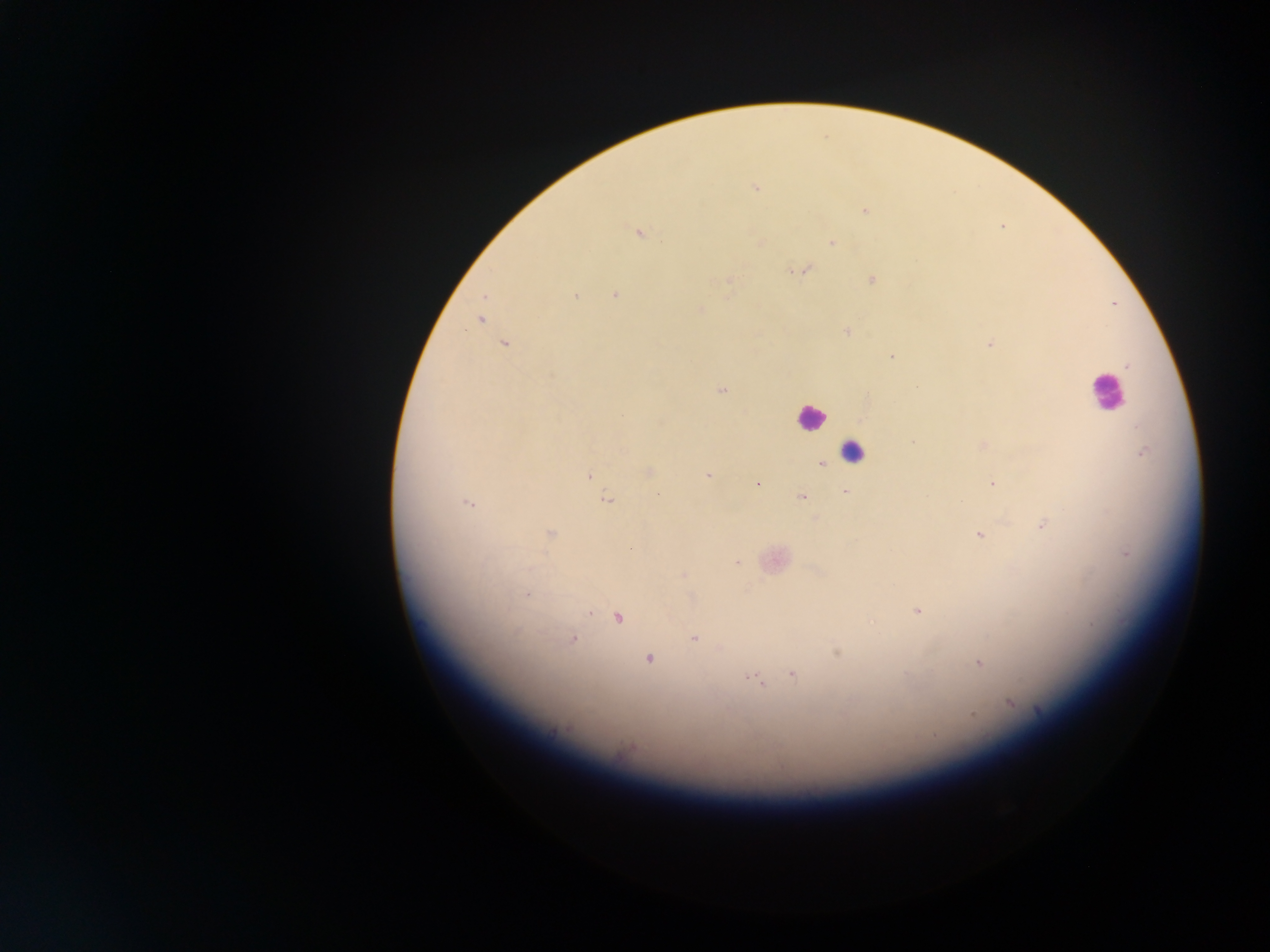

Approximate centers as [x, y] in pixels.
Summary:
  - Plasmodium parasite locations: [755, 188], [865, 210], [637, 233], [832, 242], [804, 270], [794, 271], [728, 280], [872, 280], [575, 295], [615, 295], [701, 310], [479, 320], [847, 332], [504, 344], [990, 344], [891, 357], [1127, 366], [721, 390], [913, 442], [983, 444], [1143, 452], [822, 464], [649, 471], [589, 475], [707, 476], [992, 483], [757, 484], [844, 492], [801, 496], [607, 500], [468, 502], [1042, 525], [550, 533], [980, 534], [631, 548], [737, 562], [684, 575], [525, 595], [918, 611], [590, 613], [618, 617], [694, 638], [572, 639], [837, 652], [648, 659], [978, 664], [793, 675], [750, 677], [756, 680], [761, 685], [1011, 703], [1038, 711], [972, 715], [934, 736]
  - Leukocyte locations: [1106, 392], [810, 417], [853, 450]
  - Country: Ghana
  - Capture: mobile-phone photograph through a microscope
  - Preparation: thick blood film
  - Image size: 1270×952 pixels
  - Field of view: single